Name the blood parasite species.
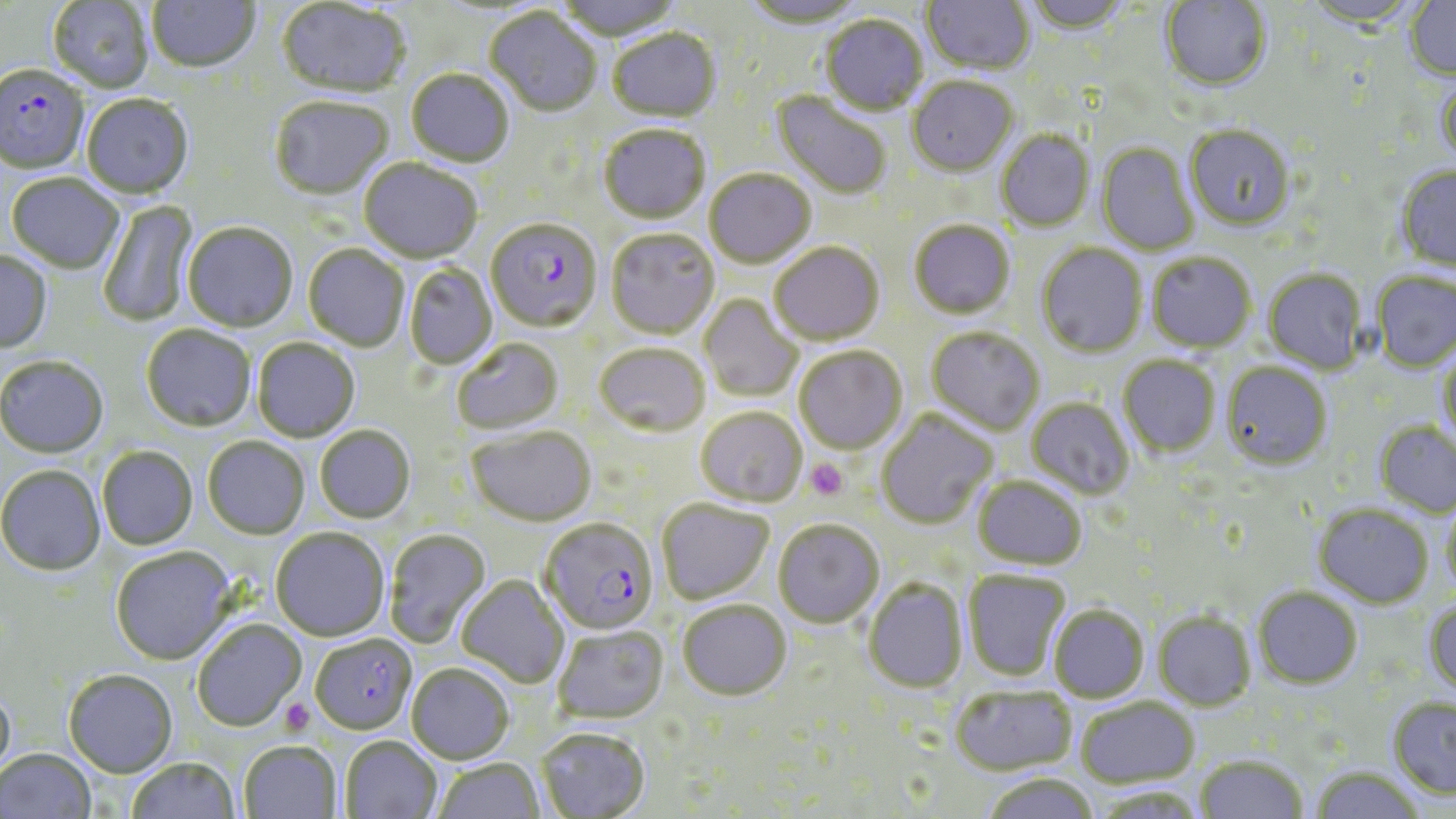
Plasmodium falciparum.

Summary:
  - Coordinate format: approximate bounding boxes as named x1/y1/x2/y2 corners in pixels
  - Uninfected red blood cell locations: (x1=48, y1=0, x2=154, y2=94), (x1=148, y1=0, x2=260, y2=75), (x1=554, y1=0, x2=683, y2=43), (x1=741, y1=0, x2=865, y2=31), (x1=922, y1=0, x2=1034, y2=76), (x1=1022, y1=0, x2=1132, y2=36), (x1=1160, y1=0, x2=1272, y2=93), (x1=1301, y1=0, x2=1424, y2=30), (x1=1405, y1=0, x2=1456, y2=81), (x1=276, y1=1, x2=409, y2=100), (x1=485, y1=9, x2=602, y2=118), (x1=821, y1=16, x2=927, y2=116), (x1=607, y1=29, x2=721, y2=124), (x1=406, y1=70, x2=515, y2=169), (x1=1437, y1=77, x2=1456, y2=168), (x1=907, y1=78, x2=1018, y2=178), (x1=771, y1=91, x2=892, y2=201), (x1=82, y1=96, x2=194, y2=201), (x1=269, y1=98, x2=393, y2=202), (x1=1185, y1=124, x2=1295, y2=231), (x1=599, y1=125, x2=710, y2=225), (x1=996, y1=130, x2=1095, y2=232), (x1=1096, y1=142, x2=1200, y2=256), (x1=359, y1=159, x2=483, y2=264), (x1=1396, y1=166, x2=1456, y2=272), (x1=704, y1=169, x2=817, y2=269), (x1=6, y1=175, x2=125, y2=274), (x1=97, y1=198, x2=200, y2=327), (x1=909, y1=220, x2=1015, y2=319), (x1=183, y1=223, x2=298, y2=333), (x1=605, y1=229, x2=719, y2=339), (x1=770, y1=242, x2=884, y2=345), (x1=1037, y1=243, x2=1148, y2=358), (x1=303, y1=245, x2=409, y2=352), (x1=0, y1=250, x2=53, y2=354), (x1=1147, y1=252, x2=1256, y2=352), (x1=404, y1=263, x2=497, y2=370), (x1=1263, y1=268, x2=1366, y2=374), (x1=1372, y1=271, x2=1456, y2=372), (x1=700, y1=294, x2=804, y2=402), (x1=141, y1=325, x2=256, y2=433), (x1=927, y1=326, x2=1045, y2=435), (x1=252, y1=338, x2=360, y2=443), (x1=452, y1=338, x2=564, y2=435), (x1=594, y1=343, x2=710, y2=436), (x1=1438, y1=346, x2=1456, y2=448), (x1=794, y1=347, x2=907, y2=455), (x1=1118, y1=355, x2=1220, y2=457), (x1=0, y1=357, x2=109, y2=460), (x1=1221, y1=361, x2=1332, y2=469), (x1=1027, y1=397, x2=1134, y2=499), (x1=696, y1=407, x2=807, y2=506), (x1=876, y1=409, x2=999, y2=528), (x1=1375, y1=422, x2=1456, y2=518), (x1=315, y1=425, x2=415, y2=524), (x1=467, y1=426, x2=596, y2=526), (x1=202, y1=437, x2=310, y2=540), (x1=97, y1=447, x2=197, y2=551), (x1=0, y1=466, x2=105, y2=577), (x1=973, y1=476, x2=1087, y2=569), (x1=657, y1=499, x2=774, y2=605), (x1=1441, y1=500, x2=1456, y2=597), (x1=1313, y1=504, x2=1433, y2=608), (x1=774, y1=519, x2=884, y2=628), (x1=271, y1=528, x2=389, y2=641), (x1=385, y1=528, x2=491, y2=648), (x1=111, y1=547, x2=236, y2=666), (x1=962, y1=569, x2=1071, y2=681), (x1=457, y1=575, x2=568, y2=689), (x1=864, y1=578, x2=968, y2=692), (x1=1254, y1=586, x2=1363, y2=688), (x1=678, y1=600, x2=791, y2=700), (x1=1424, y1=600, x2=1456, y2=696), (x1=1049, y1=604, x2=1148, y2=703), (x1=1153, y1=611, x2=1256, y2=711), (x1=191, y1=619, x2=306, y2=733), (x1=553, y1=625, x2=668, y2=724), (x1=407, y1=664, x2=514, y2=764), (x1=63, y1=670, x2=177, y2=778), (x1=0, y1=685, x2=16, y2=783), (x1=950, y1=686, x2=1076, y2=776), (x1=1075, y1=697, x2=1200, y2=789), (x1=1388, y1=698, x2=1456, y2=798), (x1=536, y1=727, x2=650, y2=819), (x1=341, y1=736, x2=442, y2=819), (x1=239, y1=741, x2=342, y2=819), (x1=0, y1=748, x2=97, y2=819), (x1=1195, y1=755, x2=1308, y2=818), (x1=126, y1=758, x2=240, y2=819), (x1=434, y1=758, x2=545, y2=819), (x1=1310, y1=767, x2=1426, y2=819), (x1=981, y1=773, x2=1099, y2=819)
  - Platelet locations: (x1=805, y1=458, x2=848, y2=501), (x1=279, y1=697, x2=314, y2=735)
  - Plasmodium falciparum-infected red blood cell locations: (x1=0, y1=66, x2=90, y2=176), (x1=486, y1=219, x2=602, y2=332), (x1=540, y1=518, x2=658, y2=636), (x1=310, y1=634, x2=418, y2=735)
  - Modality: optical microscopy
  - Preparation: thin blood film
  - Image size: 1456×819 pixels
  - Stain: May-Grünwald-Giemsa
  - Magnification: 1000x
  - Field of view: one of a larger specimen